Identify the cell.
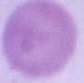

This is an erythrocyte.

modality = micrograph
magnification = 1000x